Locate and identify every blood parasite.
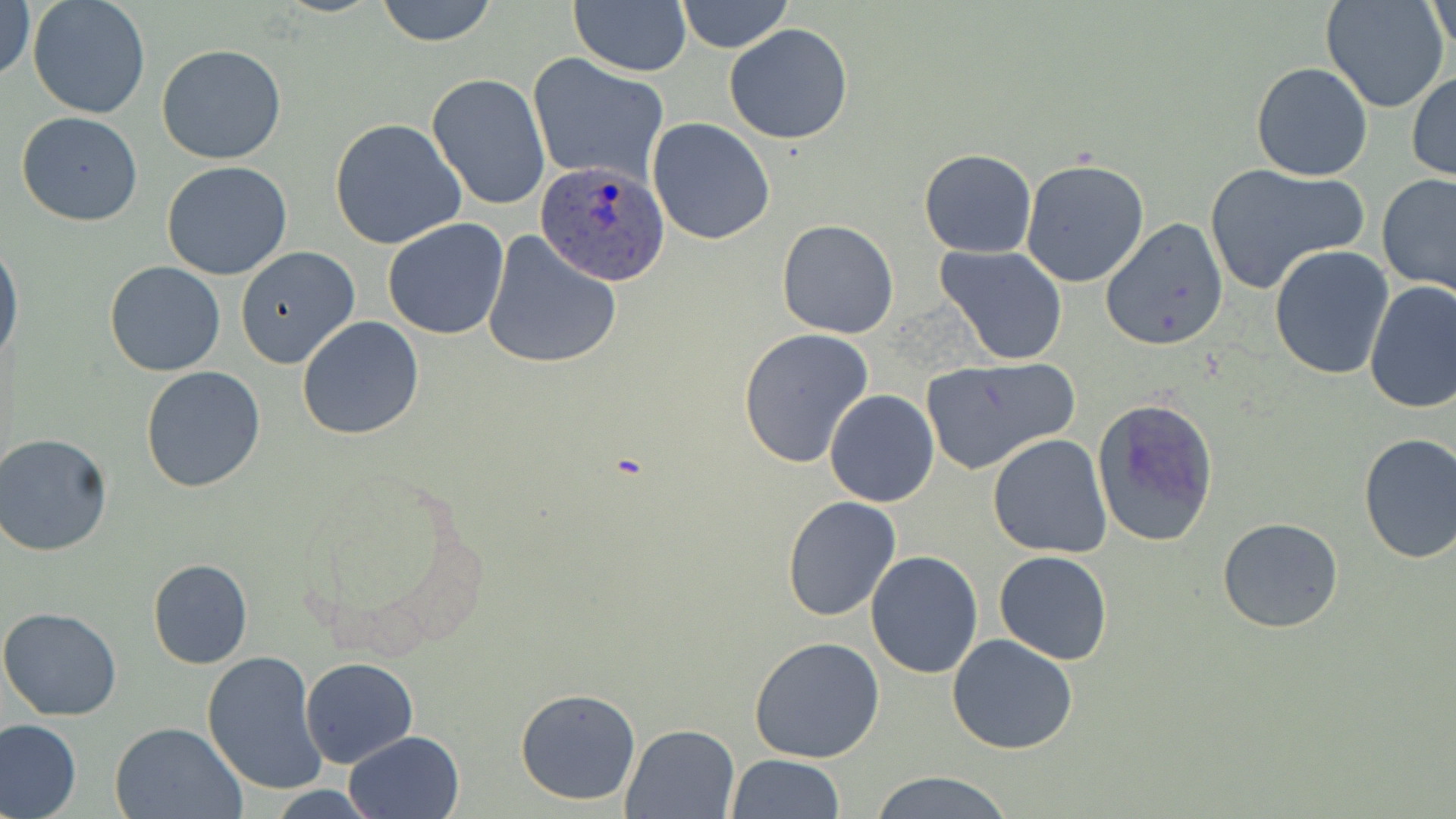
Approximate bounding boxes as named x1/y1/x2/y2 corners in pixels.
Plasmodium ovale-infected red blood cells: (x1=535, y1=161, x2=671, y2=284).
No Plasmodium falciparum, Plasmodium malariae, Plasmodium vivax, Babesia divergens, or Trypanosoma brucei observed.

Uninfected red blood cell locations: (x1=377, y1=0, x2=496, y2=47), (x1=676, y1=0, x2=792, y2=53), (x1=1321, y1=0, x2=1450, y2=113), (x1=1427, y1=0, x2=1454, y2=61), (x1=1, y1=1, x2=35, y2=86), (x1=570, y1=2, x2=690, y2=77), (x1=29, y1=3, x2=149, y2=119), (x1=723, y1=23, x2=854, y2=145), (x1=156, y1=43, x2=287, y2=165), (x1=528, y1=53, x2=669, y2=185), (x1=1250, y1=62, x2=1375, y2=182), (x1=1407, y1=70, x2=1456, y2=182), (x1=428, y1=73, x2=550, y2=213), (x1=15, y1=112, x2=145, y2=225), (x1=647, y1=117, x2=776, y2=245), (x1=329, y1=118, x2=468, y2=252), (x1=918, y1=149, x2=1037, y2=258), (x1=1020, y1=158, x2=1151, y2=288), (x1=161, y1=161, x2=293, y2=279), (x1=1204, y1=164, x2=1367, y2=295), (x1=1377, y1=173, x2=1456, y2=296), (x1=1098, y1=217, x2=1229, y2=351), (x1=382, y1=218, x2=510, y2=339), (x1=775, y1=219, x2=899, y2=339), (x1=482, y1=232, x2=624, y2=369), (x1=0, y1=241, x2=23, y2=370), (x1=936, y1=245, x2=1068, y2=364), (x1=1269, y1=245, x2=1396, y2=380), (x1=234, y1=247, x2=360, y2=369), (x1=105, y1=261, x2=225, y2=378), (x1=1364, y1=281, x2=1456, y2=414), (x1=296, y1=316, x2=424, y2=441), (x1=737, y1=329, x2=875, y2=470), (x1=920, y1=357, x2=1077, y2=474), (x1=140, y1=366, x2=267, y2=493), (x1=825, y1=390, x2=940, y2=508), (x1=1092, y1=397, x2=1220, y2=548), (x1=1, y1=433, x2=117, y2=558), (x1=987, y1=434, x2=1113, y2=558), (x1=1357, y1=434, x2=1456, y2=564), (x1=782, y1=495, x2=901, y2=621), (x1=1217, y1=517, x2=1345, y2=634), (x1=992, y1=550, x2=1113, y2=665), (x1=865, y1=551, x2=983, y2=679), (x1=147, y1=558, x2=253, y2=669), (x1=0, y1=607, x2=121, y2=720), (x1=946, y1=634, x2=1079, y2=755), (x1=749, y1=637, x2=885, y2=763), (x1=202, y1=651, x2=329, y2=795), (x1=300, y1=657, x2=418, y2=769), (x1=514, y1=686, x2=642, y2=807), (x1=0, y1=718, x2=81, y2=818), (x1=109, y1=721, x2=245, y2=819), (x1=622, y1=723, x2=739, y2=817), (x1=344, y1=729, x2=465, y2=819), (x1=726, y1=753, x2=845, y2=818), (x1=864, y1=774, x2=1016, y2=819). Slide-level diagnosis: Plasmodium ovale. Image is 1456×819 pixels. May-Grünwald-Giemsa-stained preparation. Single field of view. Thin blood smear. 1000x magnification. Optical microscopy.